Give the position of every Plasmodium parasite visible.
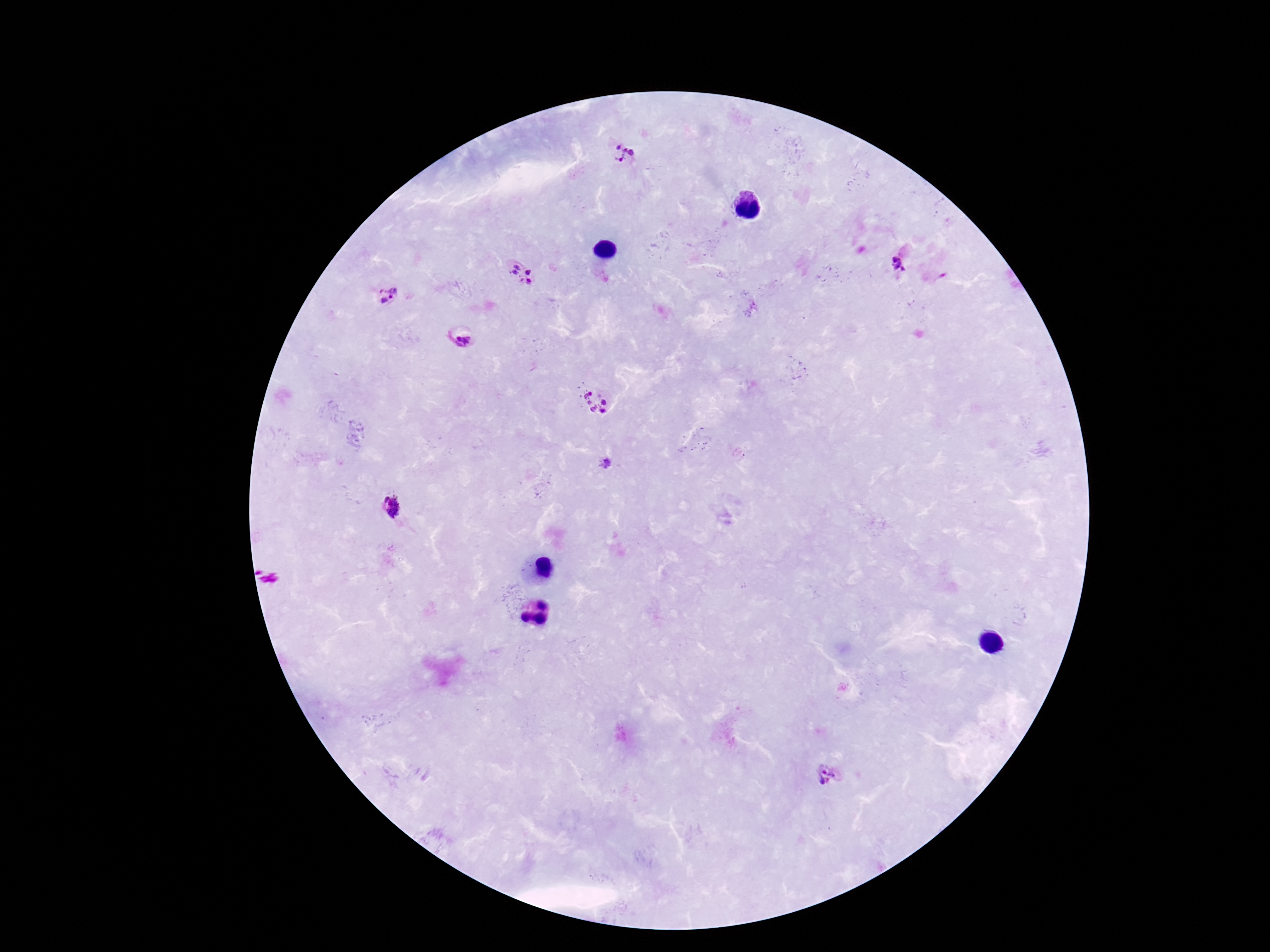
Approximate centers as (x, y) in pixels.
Plasmodium parasites: (624, 155), (517, 264), (898, 264), (529, 270), (512, 274), (530, 283), (386, 295), (464, 337), (595, 401), (607, 464), (390, 509), (828, 774).

Summary:
  - Capture: smartphone camera through the microscope eyepiece
  - Stain: Giemsa
  - Patient malaria status: infected
  - Magnification: 100x
  - Field of view: single
  - Image size: 1270×952 pixels
  - Preparation: thick peripheral-blood smear